Locate every blood parasite and identify its species.
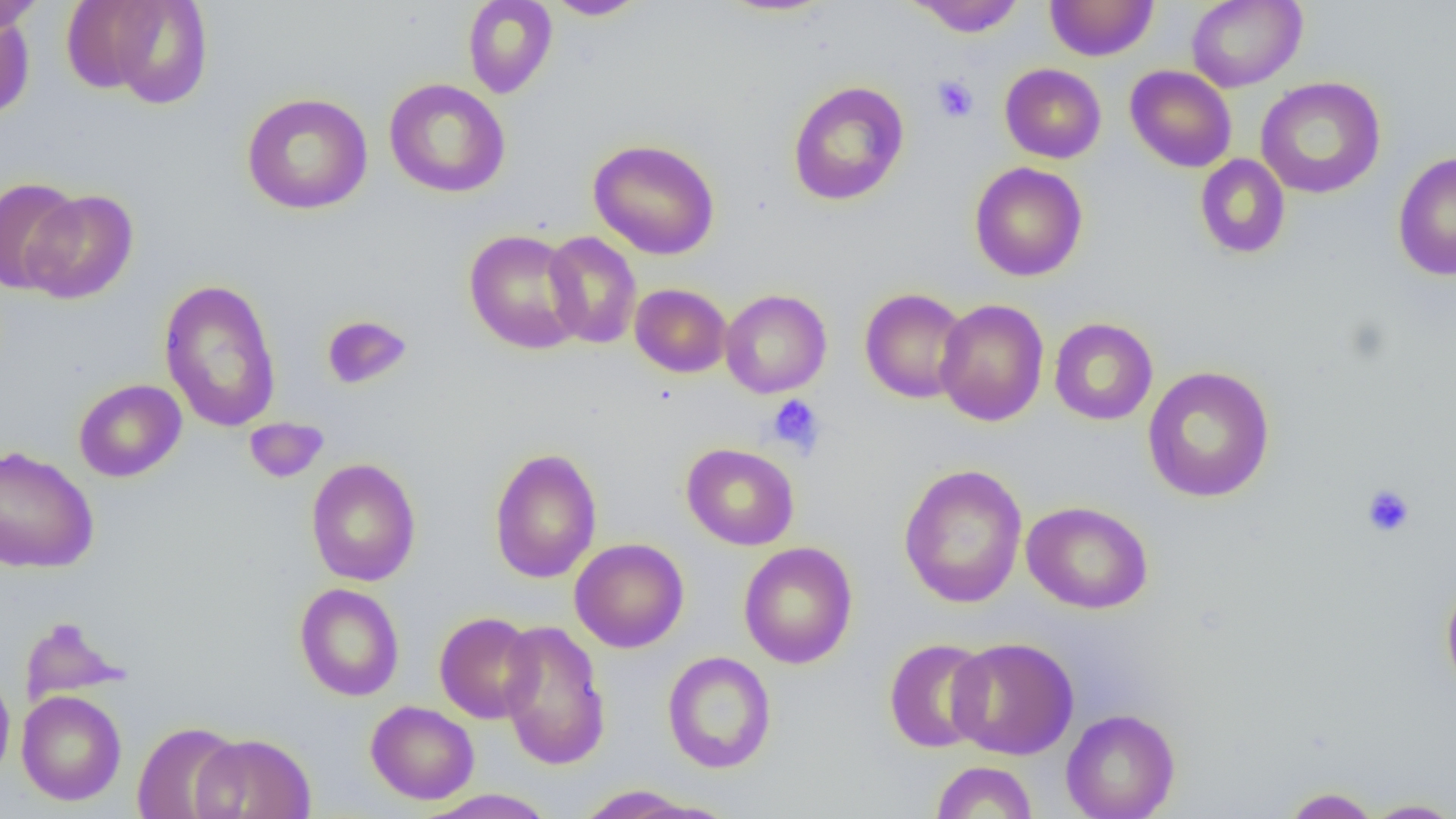

No blood parasites seen.

{
  "slide_level_diagnosis": "no evidence of blood parasites",
  "magnification": "1000x",
  "image_size": "1456×819 pixels",
  "modality": "light microscopy",
  "uninfected_red_blood_cell_locations": "approximate bounding boxes as (x1,y1)-(x2,y2) corner pairs in pixels: (77,0)-(215,110), (462,0)-(558,99), (544,0)-(647,20), (715,0)-(839,17), (907,0)-(1026,37), (1186,0)-(1307,91), (0,1)-(44,35), (1045,1)-(1159,61), (0,11)-(35,120), (1000,63)-(1106,163), (1125,65)-(1237,173), (1255,76)-(1386,199), (384,78)-(510,197), (787,80)-(910,206), (241,92)-(373,215), (588,139)-(721,260), (1392,150)-(1456,281), (1194,154)-(1291,259), (969,161)-(1088,282), (0,176)-(83,295), (22,188)-(138,304), (464,229)-(586,355), (542,232)-(642,349), (158,278)-(282,433), (630,283)-(732,377), (859,288)-(971,404), (720,289)-(832,398), (935,298)-(1049,427), (320,314)-(413,390), (1049,317)-(1158,425), (1142,366)-(1275,502), (73,379)-(187,482), (244,417)-(328,483), (681,443)-(800,550), (0,445)-(99,574), (488,447)-(602,584), (305,458)-(421,586), (898,463)-(1027,607), (1022,501)-(1154,614), (569,538)-(689,653), (738,541)-(858,669), (1441,578)-(1456,697), (294,582)-(404,701), (434,612)-(540,723), (18,617)-(129,707), (497,619)-(611,770), (947,637)-(1078,759), (883,638)-(994,753), (662,651)-(777,773), (0,670)-(15,783), (17,690)-(127,805), (366,700)-(479,804), (1061,708)-(1180,819), (132,721)-(244,819), (191,732)-(317,819), (930,761)-(1038,818), (575,784)-(707,817), (1280,787)-(1381,818), (417,789)-(558,818), (1361,798)-(1456,818)",
  "preparation": "thin blood smear",
  "platelet_locations": "approximate bounding boxes as (x1,y1)-(x2,y2) corner pairs in pixels: (932,76)-(979,123), (767,394)-(825,456), (1362,485)-(1415,537)",
  "field_of_view": "one of a larger specimen"
}